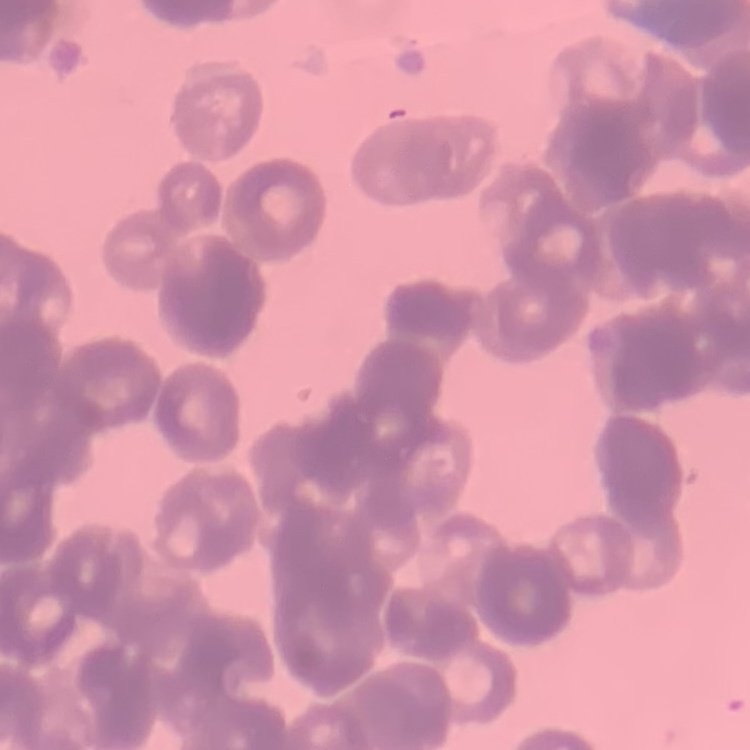
erythrocyte morphology = rouleaux formation
image type = one tile cut from a larger photomicrograph
preparation = thin blood smear
stain = Field's or Giemsa